Name the parasite shown.
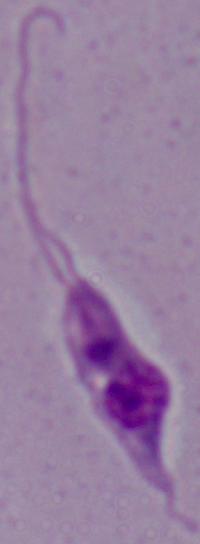
This is Leishmania.

1000x magnification. Photomicrograph.